Classify this cell by malaria status.
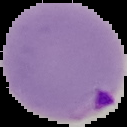
It is parasitized.

Segmented cell region on a black background. From a thin blood smear. Image is 127×127 pixels.